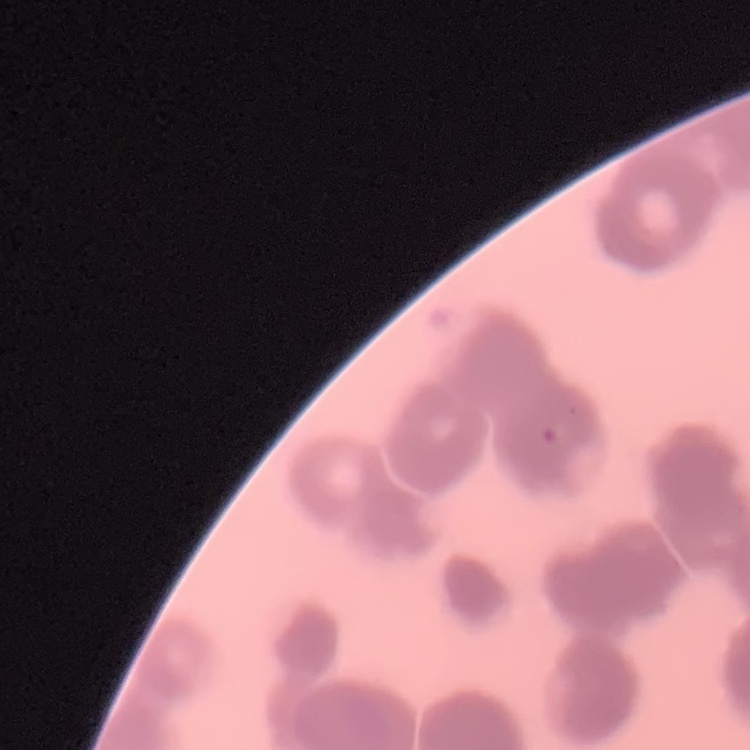
The red blood cells show rouleaux formation. Field's or Giemsa stain. Thin blood film. One tile cut from a larger photomicrograph.